Locate every Plasmodium ovale-infected red blood cell.
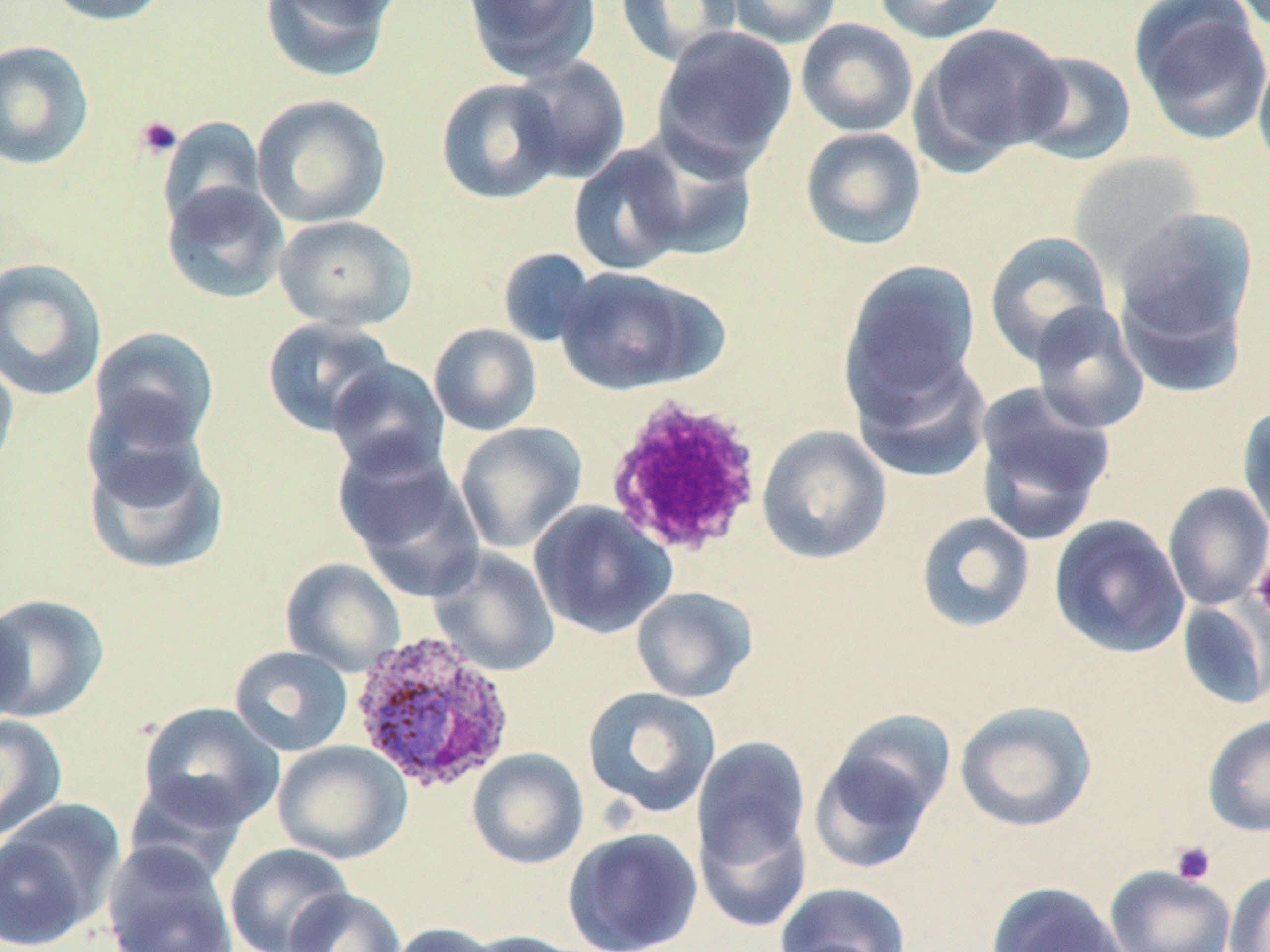

Approximate bounding boxes as (x1, y1, x2, y2) in pixels.
Plasmodium ovale-infected red blood cells: (348, 629, 518, 794).

Summary:
  - Uninfected red blood cell locations: (42, 0, 171, 26), (258, 0, 401, 83), (462, 0, 602, 81), (615, 0, 742, 68), (716, 0, 844, 48), (872, 0, 1008, 43), (1131, 2, 1270, 144), (795, 18, 919, 137), (912, 23, 1070, 169), (651, 25, 798, 175), (0, 40, 96, 171), (1253, 48, 1270, 176), (1015, 49, 1137, 165), (510, 55, 631, 183), (435, 77, 566, 205), (251, 93, 391, 228), (157, 116, 267, 230), (799, 127, 926, 251), (624, 128, 760, 263), (568, 144, 693, 276), (1066, 151, 1205, 274), (161, 180, 291, 304), (1114, 206, 1259, 364), (274, 214, 417, 332), (983, 231, 1115, 366), (497, 247, 598, 348), (0, 257, 108, 401), (840, 259, 982, 412), (554, 266, 717, 396), (1028, 302, 1150, 434), (261, 317, 396, 437), (428, 322, 542, 436), (88, 326, 220, 454), (0, 347, 20, 478), (848, 347, 993, 483), (326, 359, 450, 479), (972, 381, 1117, 546), (1237, 402, 1270, 536), (455, 422, 587, 554), (757, 425, 892, 565), (83, 432, 228, 576), (337, 445, 485, 600), (1163, 482, 1270, 610), (528, 500, 676, 640), (915, 511, 1036, 633), (1049, 514, 1190, 659), (428, 546, 560, 678), (280, 557, 405, 676), (630, 586, 758, 703), (0, 593, 109, 723), (1177, 598, 1270, 710), (0, 603, 24, 732), (229, 645, 354, 757), (581, 686, 722, 818), (954, 700, 1097, 833), (138, 702, 284, 831), (1202, 714, 1270, 837), (0, 715, 67, 842), (808, 723, 951, 876), (692, 736, 811, 882), (272, 740, 411, 864), (467, 748, 589, 870), (124, 775, 251, 885), (694, 806, 811, 934), (0, 813, 112, 951), (562, 827, 703, 952), (102, 843, 238, 952), (224, 843, 354, 952), (1104, 864, 1236, 952), (1225, 871, 1270, 952), (986, 881, 1129, 952), (773, 882, 911, 952), (283, 888, 405, 952), (387, 922, 504, 952), (461, 930, 595, 952)
  - Platelet locations: (135, 115, 183, 159), (602, 393, 765, 559), (1250, 555, 1270, 619), (1170, 841, 1216, 885)
  - Slide-level diagnosis: Plasmodium ovale
  - Field of view: one of a larger specimen
  - Stain: May-Grünwald-Giemsa
  - Magnification: 1000x
  - Image size: 1270×952 pixels
  - Preparation: thin blood film
  - Modality: optical microscopy